Outline each blood parasite and name the species.
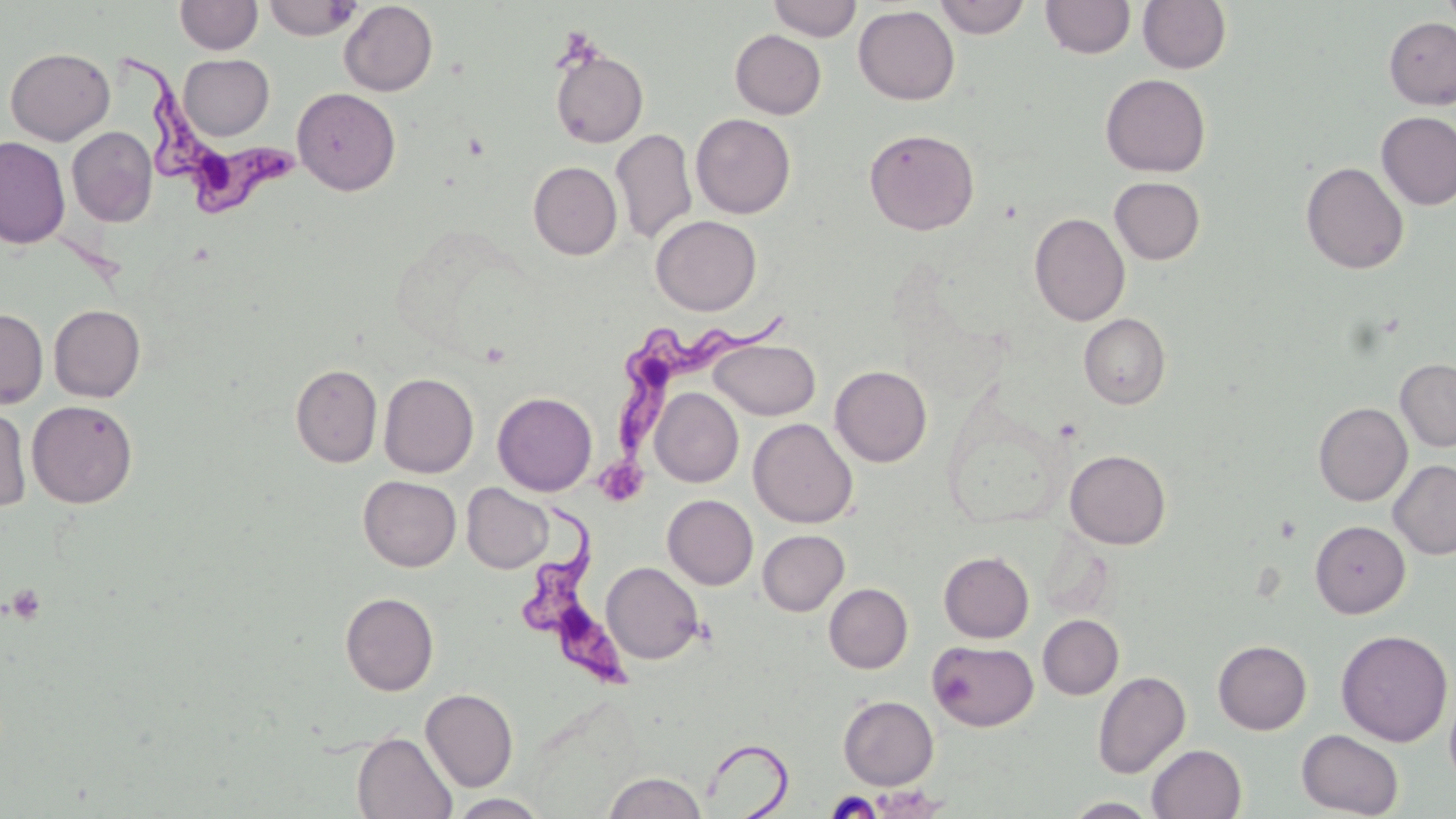
Approximate bounding boxes as named x1/y1/x2/y2 corners in pixels.
Trypanosoma brucei: (x1=117, y1=37, x2=307, y2=218), (x1=613, y1=310, x2=798, y2=459), (x1=521, y1=503, x2=630, y2=688).
No Plasmodium falciparum, Plasmodium ovale, Plasmodium malariae, Plasmodium vivax, or Babesia divergens observed.

Summary:
  - Platelet locations: (x1=599, y1=456, x2=649, y2=507), (x1=5, y1=583, x2=47, y2=624)
  - Uninfected red blood cell locations: (x1=175, y1=0, x2=263, y2=55), (x1=263, y1=0, x2=361, y2=40), (x1=767, y1=0, x2=862, y2=41), (x1=933, y1=0, x2=1031, y2=38), (x1=1041, y1=0, x2=1135, y2=59), (x1=1138, y1=0, x2=1232, y2=74), (x1=1441, y1=0, x2=1455, y2=32), (x1=339, y1=1, x2=438, y2=96), (x1=853, y1=5, x2=960, y2=105), (x1=1384, y1=17, x2=1456, y2=109), (x1=730, y1=29, x2=826, y2=119), (x1=5, y1=47, x2=115, y2=145), (x1=550, y1=48, x2=649, y2=149), (x1=178, y1=54, x2=274, y2=140), (x1=1100, y1=73, x2=1210, y2=177), (x1=292, y1=87, x2=400, y2=195), (x1=1376, y1=111, x2=1456, y2=211), (x1=691, y1=113, x2=796, y2=218), (x1=67, y1=126, x2=158, y2=227), (x1=611, y1=128, x2=697, y2=245), (x1=864, y1=128, x2=980, y2=235), (x1=0, y1=136, x2=70, y2=249), (x1=528, y1=161, x2=622, y2=260), (x1=1300, y1=161, x2=1409, y2=274), (x1=1109, y1=177, x2=1205, y2=264), (x1=1029, y1=212, x2=1130, y2=326), (x1=651, y1=215, x2=761, y2=315), (x1=49, y1=304, x2=145, y2=402), (x1=0, y1=308, x2=48, y2=409), (x1=1079, y1=313, x2=1170, y2=409), (x1=710, y1=339, x2=820, y2=420), (x1=1396, y1=359, x2=1456, y2=451), (x1=290, y1=364, x2=382, y2=468), (x1=830, y1=365, x2=932, y2=467), (x1=379, y1=373, x2=478, y2=477), (x1=650, y1=387, x2=743, y2=487), (x1=492, y1=391, x2=597, y2=495), (x1=27, y1=400, x2=138, y2=508), (x1=1314, y1=402, x2=1412, y2=505), (x1=0, y1=405, x2=32, y2=513), (x1=748, y1=418, x2=857, y2=527), (x1=1065, y1=449, x2=1171, y2=549), (x1=1388, y1=459, x2=1456, y2=560), (x1=358, y1=476, x2=461, y2=571), (x1=462, y1=483, x2=553, y2=573), (x1=662, y1=494, x2=758, y2=590), (x1=1310, y1=519, x2=1410, y2=618), (x1=758, y1=530, x2=849, y2=615), (x1=939, y1=551, x2=1034, y2=642), (x1=602, y1=562, x2=704, y2=664), (x1=824, y1=583, x2=913, y2=673), (x1=340, y1=592, x2=439, y2=695), (x1=1038, y1=614, x2=1124, y2=699), (x1=1335, y1=629, x2=1453, y2=746), (x1=928, y1=640, x2=1038, y2=731), (x1=1213, y1=640, x2=1311, y2=734), (x1=1092, y1=670, x2=1190, y2=778), (x1=1444, y1=685, x2=1456, y2=790), (x1=420, y1=688, x2=518, y2=792), (x1=838, y1=695, x2=938, y2=789), (x1=1296, y1=729, x2=1404, y2=817), (x1=351, y1=732, x2=457, y2=819), (x1=1147, y1=744, x2=1246, y2=819), (x1=603, y1=771, x2=707, y2=818), (x1=449, y1=794, x2=549, y2=818), (x1=1063, y1=797, x2=1160, y2=818)
  - Slide-level diagnosis: Trypanosoma brucei
  - Modality: light microscopy
  - Image size: 1456×819 pixels
  - Preparation: thin blood film
  - Field of view: one of a larger specimen
  - Stain: May-Grünwald-Giemsa
  - Magnification: 1000x